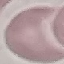
Summary:
  - Result: no malaria parasites detected
  - Preparation: thin smear
  - Image type: automatically extracted cell patch, resized to 64 × 64 pixels
  - Capture: smartphone through the microscope eyepiece
  - Stain: Giemsa